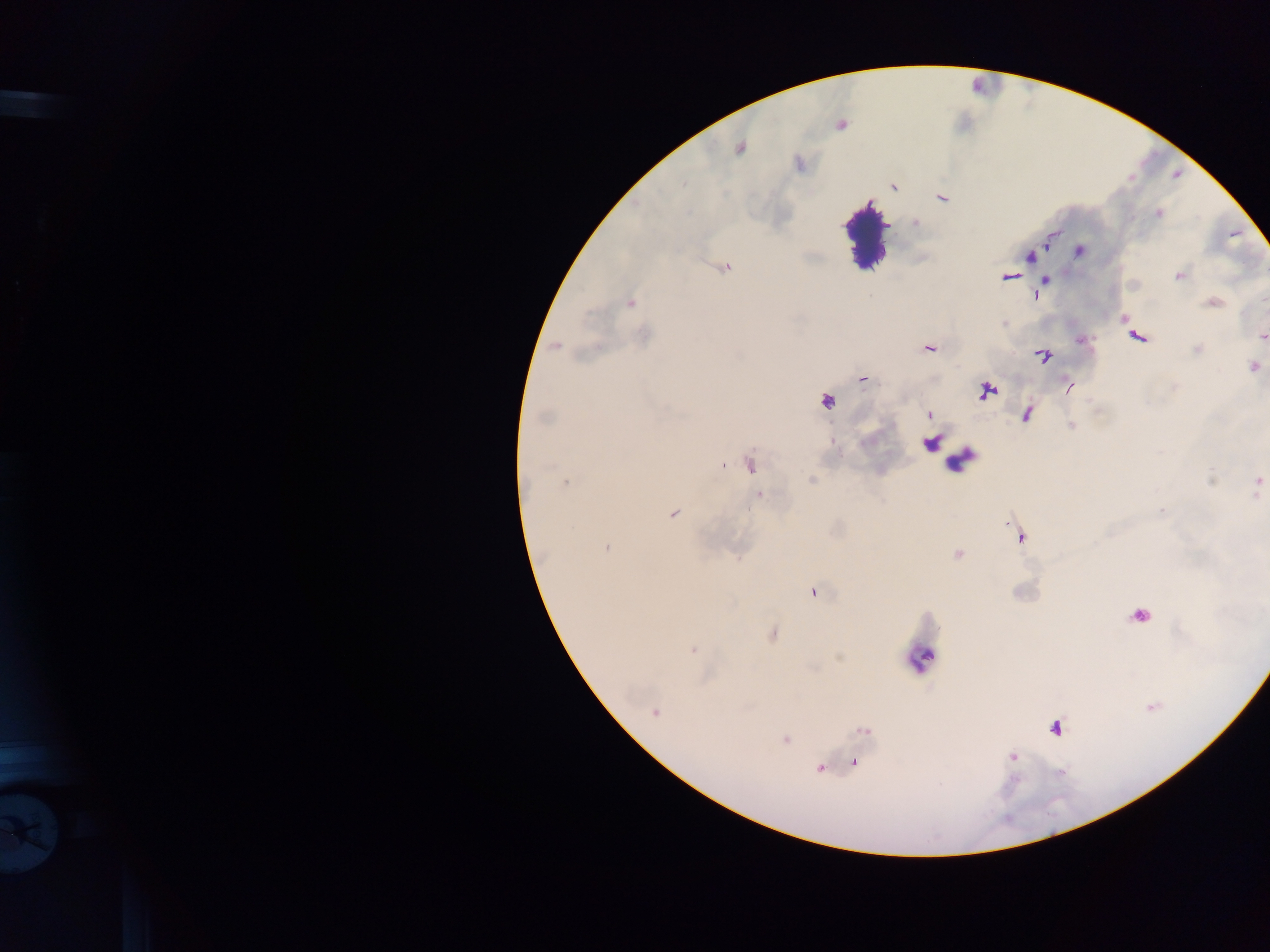
image size = 1270×952 pixels
leukocyte locations = approximate centers as [x, y] in pixels: [866, 230], [959, 460], [919, 659]
Plasmodium parasite locations = approximate centers as [x, y] in pixels: [840, 124], [740, 147], [893, 186], [942, 198], [1158, 213], [916, 223], [1048, 238], [1079, 250], [1029, 256], [724, 266], [1178, 275], [1009, 276], [1045, 280], [1035, 296], [630, 302], [1213, 303], [1125, 319], [645, 336], [1137, 336], [1262, 336], [1082, 340], [556, 346], [929, 347], [1197, 349], [1041, 355], [1253, 367], [862, 378], [1069, 386], [985, 391], [826, 400], [929, 414], [1026, 414], [544, 416], [1070, 425], [749, 464], [811, 481], [565, 482], [1258, 485], [759, 495], [1163, 511], [672, 513], [1020, 536], [606, 547], [957, 554], [813, 592], [1139, 615], [772, 634], [693, 650], [655, 712], [1055, 727], [864, 731], [785, 740], [1011, 757], [853, 762], [820, 767]
object labeled both Plasmodium parasite and leukocyte by the source = approximate centers as [x, y] in pixels: [930, 442]
country = Ghana
preparation = thick blood smear
capture = mobile-phone photograph through a microscope
field of view = single